Locate every Plasmodium parasite.
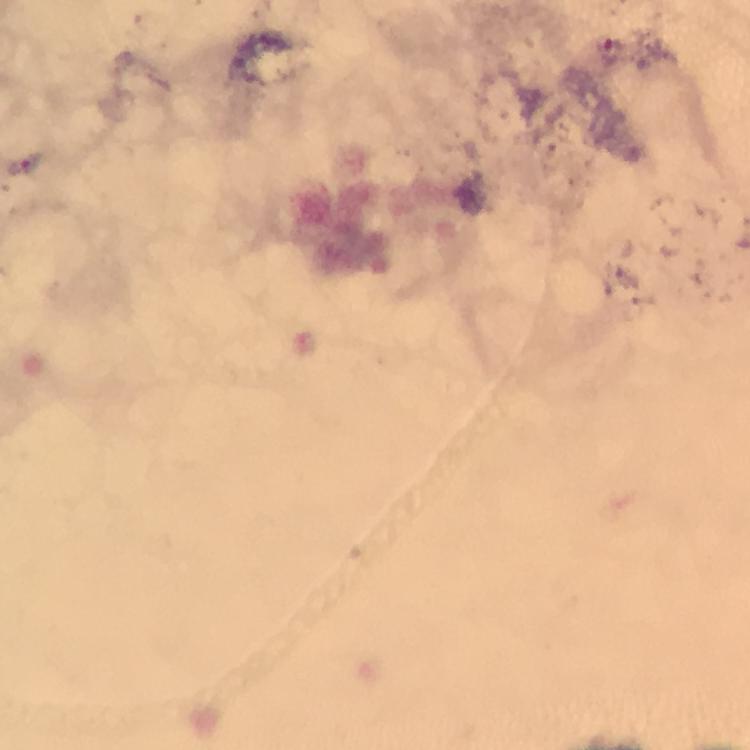

Approximate centers as (x, y) in pixels.
Plasmodium parasites: (24, 164).

Giemsa-stained preparation. 100x magnification. A crop from one field of view. Photographed with a smartphone mounted on the microscope. Image is 750×750 pixels. From a diagnostic examination for malaria. Thick blood smear. Immersion oil applied.